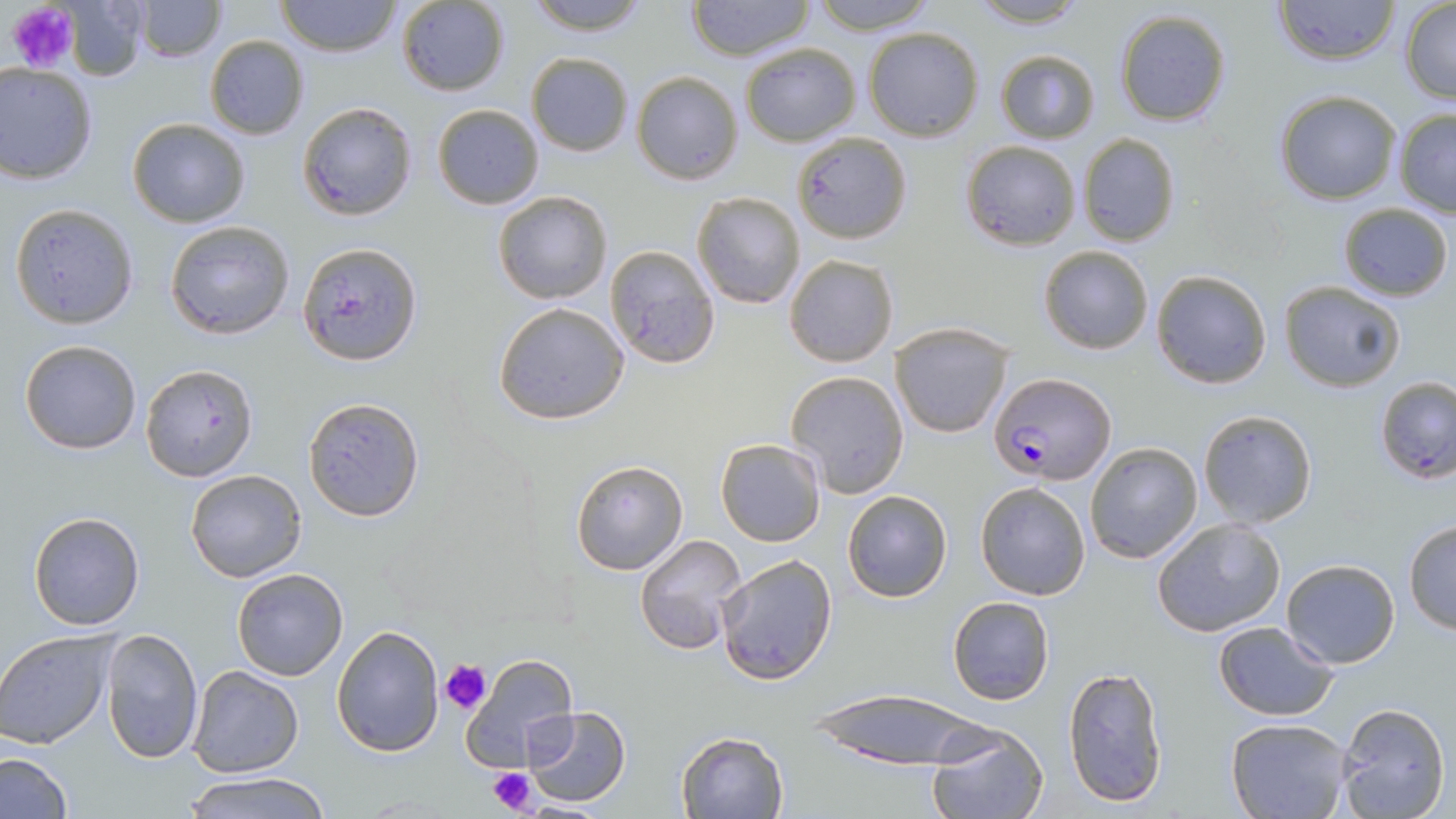

slide-level diagnosis = Plasmodium falciparum
magnification = 1000x
platelet locations = approximate bounding boxes as (x1, y1, x2, y2) in pixels: (7, 2, 79, 74), (438, 658, 493, 716), (485, 765, 541, 817)
image size = 1456×819 pixels
Plasmodium falciparum-infected red blood cell locations = approximate bounding boxes as (x1, y1, x2, y2) in pixels: (989, 372, 1115, 485)
uninfected red blood cell locations = approximate bounding boxes as (x1, y1, x2, y2) in pixels: (134, 0, 225, 62), (275, 0, 400, 58), (522, 0, 654, 36), (685, 0, 816, 60), (809, 0, 942, 34), (964, 0, 1092, 28), (1273, 0, 1400, 67), (396, 1, 510, 96), (1400, 2, 1456, 102), (59, 4, 151, 80), (1114, 9, 1232, 127), (862, 26, 983, 140), (205, 35, 310, 140), (739, 42, 862, 147), (995, 50, 1099, 145), (525, 52, 632, 158), (0, 63, 99, 184), (631, 70, 743, 186), (1272, 90, 1401, 205), (297, 101, 417, 221), (433, 103, 543, 209), (1393, 109, 1456, 216), (126, 118, 251, 227), (793, 130, 910, 245), (1077, 133, 1180, 247), (959, 139, 1082, 250), (493, 191, 612, 305), (692, 191, 807, 310), (1337, 202, 1453, 301), (10, 203, 140, 328), (163, 219, 295, 338), (296, 242, 423, 366), (604, 245, 721, 368), (1038, 245, 1153, 354), (785, 254, 897, 368), (1150, 270, 1272, 389), (1278, 281, 1405, 392), (493, 303, 629, 425), (889, 322, 1016, 439), (20, 340, 142, 454), (140, 363, 258, 481), (787, 370, 909, 497), (1374, 377, 1455, 485), (302, 395, 425, 522), (1196, 409, 1319, 528), (715, 437, 825, 548), (1085, 442, 1203, 564), (570, 458, 690, 575), (185, 468, 307, 583), (974, 481, 1091, 601), (842, 490, 952, 602), (27, 511, 146, 630), (1152, 516, 1286, 637), (1402, 519, 1456, 634), (633, 534, 747, 655), (714, 554, 836, 686), (1281, 560, 1400, 668), (230, 568, 348, 681), (947, 595, 1055, 706), (1213, 621, 1339, 720), (331, 624, 445, 758), (101, 627, 203, 765), (0, 631, 117, 748), (460, 653, 579, 771), (188, 665, 305, 778), (1063, 666, 1170, 809), (808, 689, 992, 768), (1334, 703, 1449, 819), (524, 705, 633, 806), (1226, 717, 1352, 819), (925, 722, 1049, 819), (675, 730, 789, 819), (0, 752, 74, 819), (185, 770, 330, 819)
stain = May-Grünwald-Giemsa
field of view = one of a larger specimen
preparation = thin blood smear
modality = optical microscopy